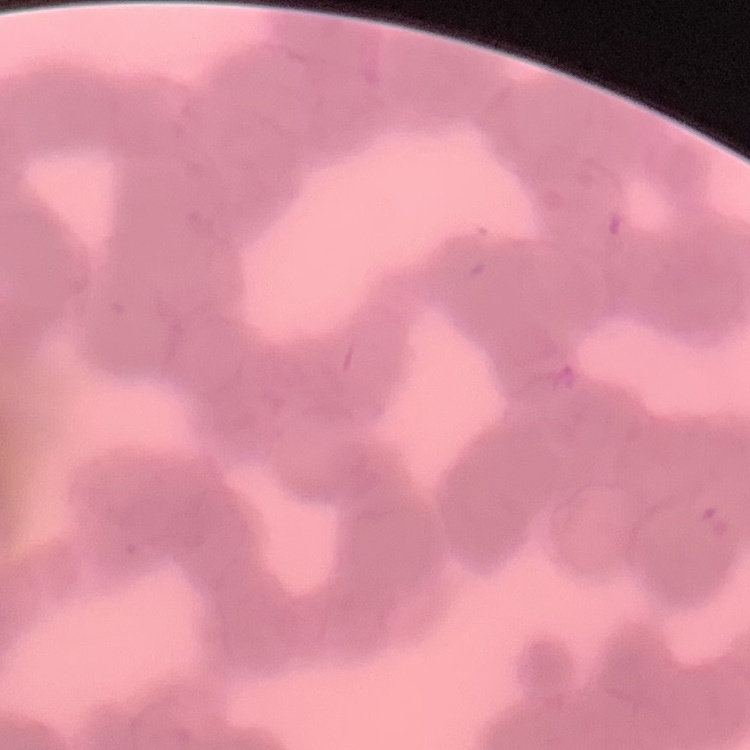
{
  "red_blood_cell_morphology": "rouleaux formation",
  "stain": "Field's or Giemsa",
  "image_type": "one tile cut from a larger photomicrograph",
  "preparation": "thin blood film"
}